Locate every uninfected red blood cell.
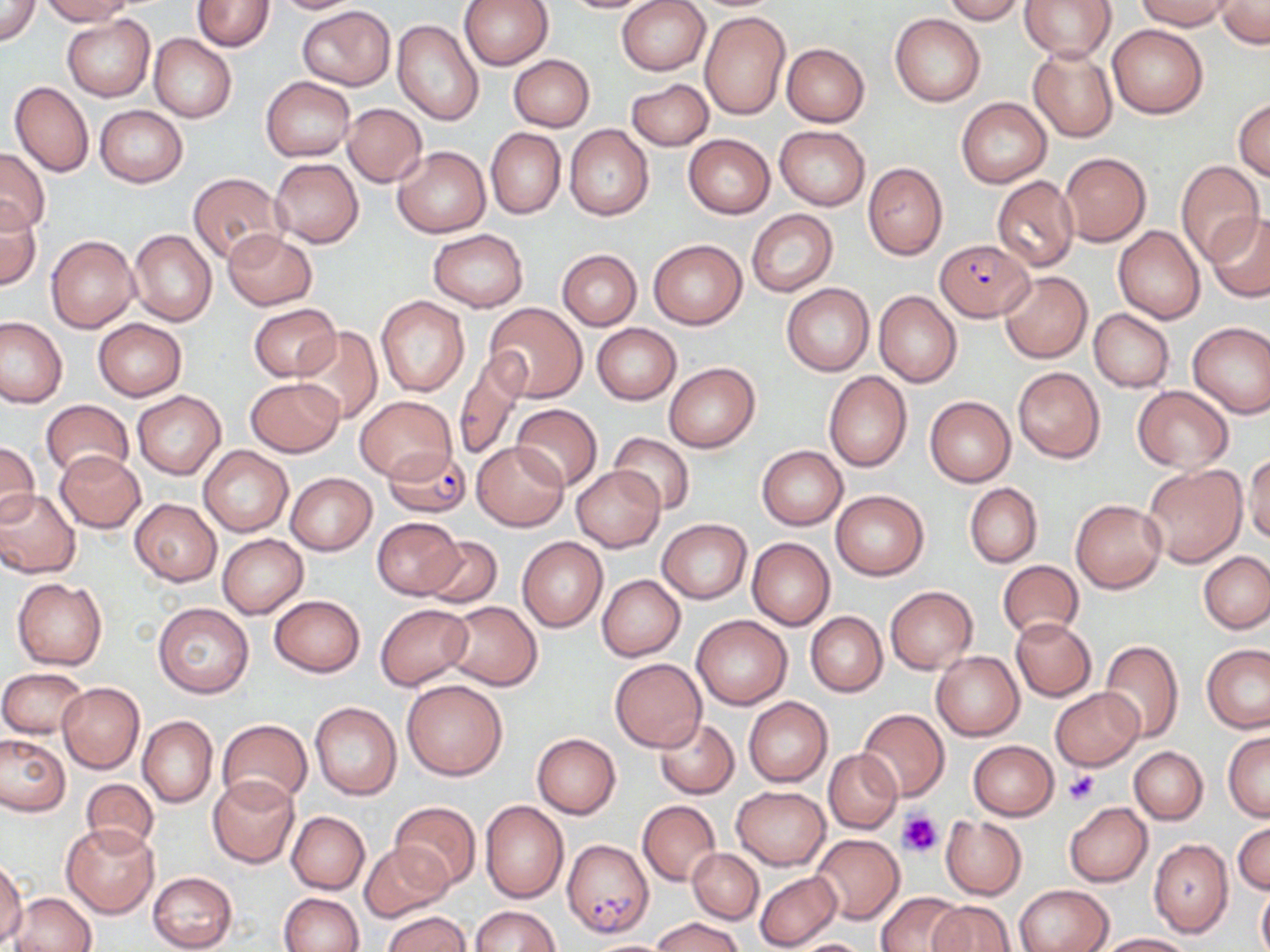
Approximate bounding boxes as named x1/y1/x2/y2 corners in pixels.
Uninfected red blood cells: (x1=1, y1=0, x2=41, y2=47), (x1=40, y1=0, x2=135, y2=24), (x1=193, y1=0, x2=273, y2=52), (x1=267, y1=0, x2=363, y2=13), (x1=458, y1=0, x2=552, y2=71), (x1=556, y1=0, x2=665, y2=14), (x1=943, y1=0, x2=1024, y2=23), (x1=1021, y1=0, x2=1115, y2=61), (x1=1136, y1=0, x2=1235, y2=31), (x1=1216, y1=0, x2=1270, y2=48), (x1=616, y1=1, x2=710, y2=76), (x1=297, y1=5, x2=396, y2=90), (x1=700, y1=10, x2=790, y2=119), (x1=890, y1=13, x2=986, y2=106), (x1=61, y1=15, x2=154, y2=102), (x1=392, y1=18, x2=484, y2=126), (x1=1108, y1=23, x2=1209, y2=118), (x1=149, y1=35, x2=236, y2=122), (x1=782, y1=44, x2=869, y2=127), (x1=1027, y1=47, x2=1118, y2=142), (x1=509, y1=54, x2=594, y2=130), (x1=260, y1=76, x2=356, y2=161), (x1=627, y1=79, x2=713, y2=151), (x1=10, y1=81, x2=93, y2=177), (x1=1233, y1=97, x2=1270, y2=181), (x1=957, y1=98, x2=1051, y2=187), (x1=342, y1=103, x2=426, y2=186), (x1=94, y1=106, x2=187, y2=187), (x1=564, y1=125, x2=653, y2=220), (x1=775, y1=126, x2=869, y2=209), (x1=486, y1=128, x2=566, y2=220), (x1=684, y1=134, x2=774, y2=217), (x1=0, y1=147, x2=51, y2=233), (x1=392, y1=147, x2=489, y2=237), (x1=1060, y1=152, x2=1152, y2=245), (x1=270, y1=158, x2=364, y2=247), (x1=1176, y1=161, x2=1266, y2=265), (x1=862, y1=162, x2=947, y2=259), (x1=187, y1=174, x2=288, y2=263), (x1=992, y1=176, x2=1078, y2=271), (x1=0, y1=201, x2=41, y2=288), (x1=747, y1=210, x2=837, y2=294), (x1=1206, y1=212, x2=1270, y2=302), (x1=1114, y1=225, x2=1205, y2=323), (x1=223, y1=228, x2=317, y2=310), (x1=128, y1=229, x2=215, y2=327), (x1=428, y1=229, x2=528, y2=311), (x1=45, y1=235, x2=140, y2=333), (x1=648, y1=239, x2=746, y2=328), (x1=558, y1=250, x2=642, y2=329), (x1=999, y1=272, x2=1093, y2=363), (x1=781, y1=282, x2=874, y2=376), (x1=873, y1=290, x2=963, y2=387), (x1=375, y1=296, x2=470, y2=397), (x1=248, y1=303, x2=341, y2=381), (x1=483, y1=304, x2=587, y2=402), (x1=1088, y1=309, x2=1174, y2=391), (x1=0, y1=317, x2=66, y2=407), (x1=93, y1=319, x2=186, y2=400), (x1=1187, y1=322, x2=1270, y2=419), (x1=592, y1=323, x2=680, y2=404), (x1=291, y1=326, x2=383, y2=424), (x1=452, y1=351, x2=528, y2=462), (x1=665, y1=362, x2=759, y2=452), (x1=1013, y1=367, x2=1104, y2=462), (x1=823, y1=370, x2=912, y2=472), (x1=246, y1=375, x2=344, y2=455), (x1=1130, y1=386, x2=1234, y2=472), (x1=134, y1=392, x2=225, y2=479), (x1=354, y1=395, x2=456, y2=483), (x1=925, y1=395, x2=1016, y2=486), (x1=40, y1=401, x2=135, y2=480), (x1=511, y1=403, x2=601, y2=489), (x1=609, y1=433, x2=696, y2=514), (x1=0, y1=439, x2=39, y2=527), (x1=473, y1=441, x2=567, y2=531), (x1=757, y1=445, x2=848, y2=530), (x1=198, y1=446, x2=293, y2=537), (x1=54, y1=450, x2=145, y2=532), (x1=1245, y1=453, x2=1270, y2=546), (x1=1142, y1=463, x2=1248, y2=568), (x1=572, y1=465, x2=664, y2=551), (x1=285, y1=472, x2=376, y2=555), (x1=964, y1=483, x2=1042, y2=568), (x1=0, y1=489, x2=81, y2=578), (x1=831, y1=490, x2=929, y2=580), (x1=130, y1=498, x2=221, y2=584), (x1=1070, y1=498, x2=1167, y2=594), (x1=372, y1=517, x2=464, y2=600), (x1=657, y1=518, x2=752, y2=603), (x1=217, y1=533, x2=308, y2=618), (x1=419, y1=534, x2=502, y2=607), (x1=516, y1=536, x2=608, y2=632), (x1=747, y1=537, x2=834, y2=630), (x1=1198, y1=551, x2=1270, y2=634), (x1=997, y1=561, x2=1084, y2=640), (x1=596, y1=575, x2=685, y2=661), (x1=12, y1=577, x2=107, y2=669), (x1=885, y1=586, x2=977, y2=673), (x1=269, y1=595, x2=366, y2=676), (x1=153, y1=602, x2=254, y2=697), (x1=444, y1=602, x2=542, y2=690), (x1=375, y1=603, x2=472, y2=689), (x1=805, y1=612, x2=886, y2=697), (x1=692, y1=615, x2=791, y2=709), (x1=1011, y1=618, x2=1095, y2=700), (x1=1100, y1=640, x2=1184, y2=741), (x1=1201, y1=644, x2=1270, y2=733), (x1=931, y1=651, x2=1025, y2=740), (x1=609, y1=657, x2=707, y2=752), (x1=1, y1=667, x2=87, y2=737), (x1=401, y1=679, x2=507, y2=779), (x1=57, y1=682, x2=145, y2=772), (x1=1051, y1=687, x2=1143, y2=769), (x1=743, y1=696, x2=833, y2=787), (x1=309, y1=702, x2=401, y2=799), (x1=856, y1=708, x2=951, y2=802), (x1=138, y1=716, x2=217, y2=808), (x1=218, y1=718, x2=312, y2=807), (x1=655, y1=718, x2=739, y2=798), (x1=1223, y1=731, x2=1270, y2=821), (x1=532, y1=732, x2=621, y2=818), (x1=0, y1=734, x2=69, y2=816), (x1=968, y1=741, x2=1058, y2=820), (x1=1129, y1=746, x2=1208, y2=824), (x1=824, y1=750, x2=901, y2=832), (x1=208, y1=777, x2=300, y2=868), (x1=80, y1=779, x2=159, y2=853), (x1=731, y1=785, x2=830, y2=869), (x1=638, y1=800, x2=720, y2=885), (x1=390, y1=801, x2=481, y2=890), (x1=480, y1=801, x2=570, y2=903), (x1=1064, y1=802, x2=1152, y2=887), (x1=286, y1=811, x2=369, y2=893), (x1=940, y1=817, x2=1026, y2=897), (x1=1233, y1=821, x2=1269, y2=895), (x1=61, y1=823, x2=159, y2=917), (x1=811, y1=834, x2=904, y2=924), (x1=1148, y1=838, x2=1234, y2=937), (x1=360, y1=843, x2=452, y2=920), (x1=688, y1=848, x2=763, y2=923), (x1=0, y1=861, x2=26, y2=945), (x1=148, y1=871, x2=238, y2=951), (x1=754, y1=871, x2=841, y2=950), (x1=1256, y1=880, x2=1270, y2=952), (x1=1015, y1=885, x2=1113, y2=952), (x1=279, y1=892, x2=363, y2=952), (x1=877, y1=892, x2=966, y2=951), (x1=8, y1=893, x2=95, y2=952), (x1=930, y1=900, x2=1014, y2=951), (x1=471, y1=906, x2=562, y2=951), (x1=382, y1=911, x2=470, y2=952), (x1=651, y1=917, x2=746, y2=952), (x1=1097, y1=933, x2=1195, y2=952), (x1=579, y1=938, x2=682, y2=951), (x1=783, y1=938, x2=875, y2=952).

Plasmodium falciparum-infected red blood cell locations: (x1=935, y1=239, x2=1034, y2=321), (x1=382, y1=445, x2=471, y2=519), (x1=562, y1=837, x2=653, y2=937). Platelet locations: (x1=1064, y1=770, x2=1100, y2=807), (x1=897, y1=810, x2=944, y2=856). Slide-level diagnosis: Plasmodium falciparum. Captured at 1000x magnification. Thin blood film. May-Grünwald-Giemsa stain. Optical microscopy. Image is 1270×952 pixels. One field of a larger specimen.